Locate every uninfected red blood cell.
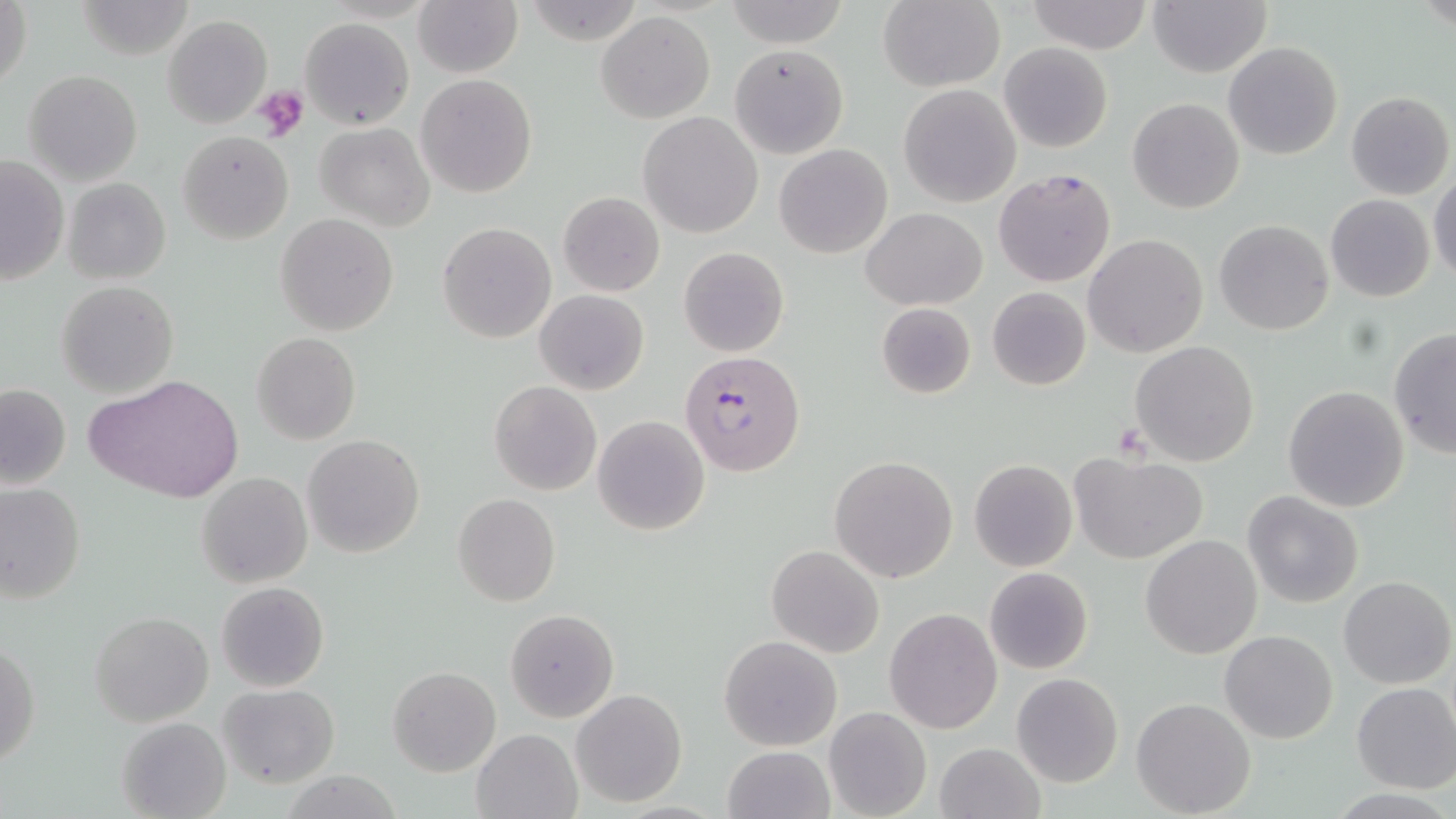

Approximate bounding boxes as [x1, y1, x2, y2] in pixels.
Uninfected red blood cells: [413, 0, 522, 77], [877, 0, 1004, 92], [1, 1, 32, 94], [723, 1, 850, 48], [1027, 1, 1151, 53], [1148, 1, 1271, 77], [597, 12, 715, 123], [163, 15, 273, 128], [300, 18, 414, 129], [1223, 41, 1343, 161], [999, 42, 1114, 152], [728, 44, 848, 158], [679, 54, 817, 198], [25, 70, 141, 185], [416, 74, 538, 198], [898, 83, 1021, 208], [1345, 91, 1454, 201], [1127, 98, 1245, 213], [637, 111, 763, 239], [315, 122, 434, 230], [177, 130, 294, 244], [774, 143, 892, 258], [0, 154, 69, 286], [994, 166, 1117, 288], [1430, 174, 1456, 283], [65, 178, 170, 284], [557, 191, 666, 297], [1326, 194, 1435, 302], [862, 207, 984, 310], [276, 213, 397, 334], [1213, 220, 1334, 336], [438, 222, 556, 345], [1085, 234, 1208, 357], [679, 247, 788, 358], [56, 280, 178, 398], [987, 287, 1091, 389], [536, 290, 648, 394], [875, 303, 976, 399], [1388, 329, 1456, 458], [251, 332, 360, 445], [1129, 340, 1261, 466], [89, 374, 244, 505], [0, 381, 71, 490], [489, 381, 602, 496], [1283, 385, 1410, 513], [592, 414, 710, 536], [302, 434, 425, 558], [1069, 451, 1207, 563], [830, 455, 957, 583], [969, 460, 1078, 572], [198, 472, 312, 589], [0, 482, 86, 604], [1242, 491, 1363, 608], [452, 493, 560, 607], [1140, 534, 1262, 659], [767, 545, 884, 657], [984, 566, 1094, 675], [1338, 575, 1455, 689], [215, 581, 329, 693], [884, 607, 1002, 733], [505, 609, 618, 721], [90, 611, 213, 727], [1220, 630, 1337, 744], [719, 636, 841, 751], [1, 639, 40, 771], [388, 666, 501, 776], [1012, 672, 1123, 788], [1351, 682, 1456, 793], [217, 683, 340, 787], [572, 690, 686, 806], [1132, 697, 1257, 818], [825, 706, 932, 819], [116, 717, 230, 818], [472, 728, 582, 818], [936, 741, 1045, 819], [722, 745, 834, 819].

slide-level diagnosis = Plasmodium falciparum
preparation = thin blood smear
field of view = single
platelet locations = approximate bounding boxes as [x1, y1, x2, y2] in pixels: [253, 84, 311, 141]
stain = May-Grünwald-Giemsa
magnification = 1000x
image size = 1456×819 pixels
Plasmodium falciparum-infected red blood cell locations = approximate bounding boxes as [x1, y1, x2, y2] in pixels: [681, 351, 805, 476]
modality = optical microscopy